Identify the parasite.
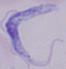

This is a trypanosome.

modality: photomicrograph
magnification: 1000x